Locate every blood parasite and identify its species.
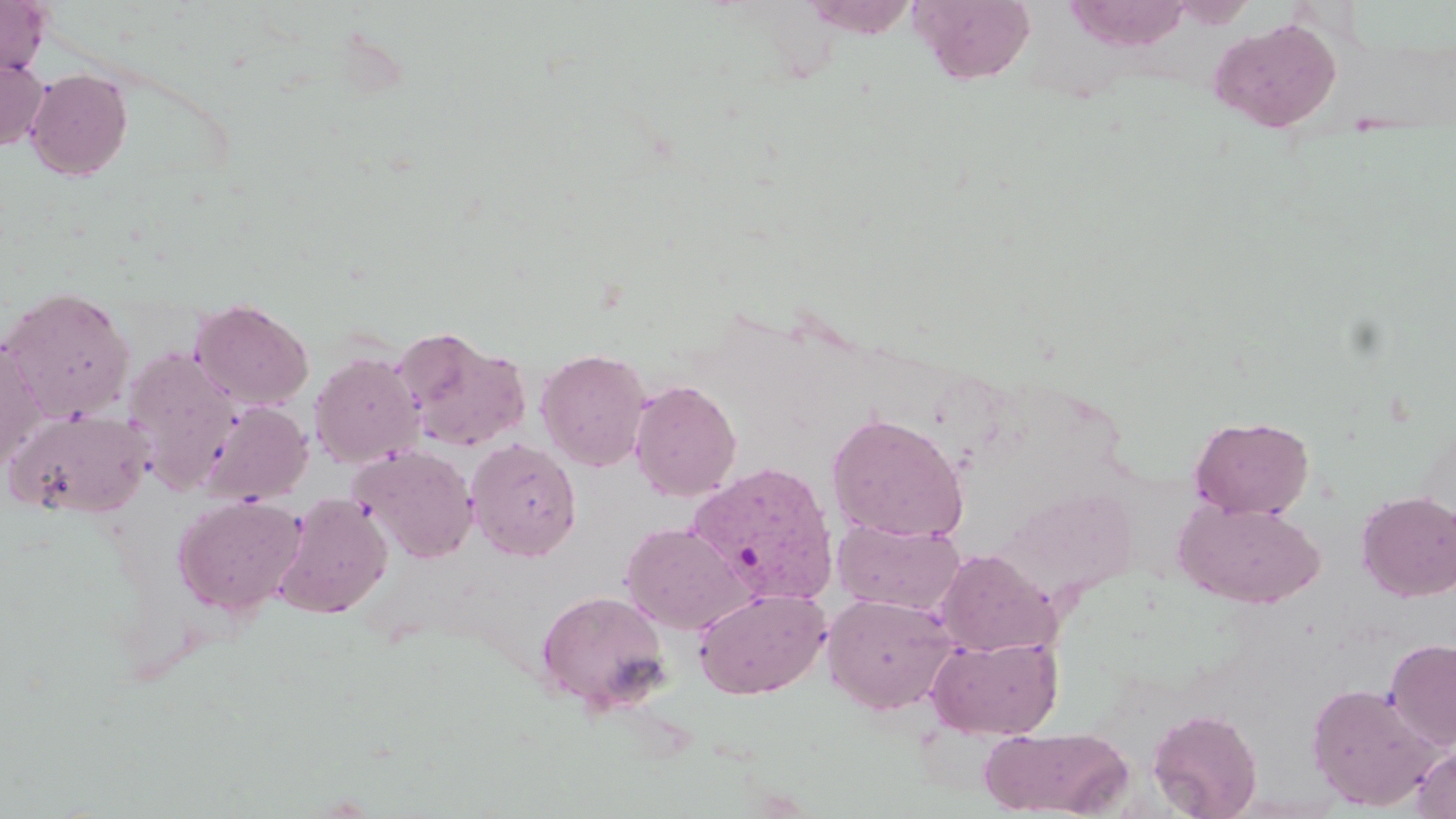

Approximate bounding boxes as [x1, y1, x2, y2] in pixels.
Plasmodium vivax-infected red blood cells: [687, 461, 839, 606].
No Plasmodium falciparum, Plasmodium ovale, Plasmodium malariae, Babesia divergens, or Trypanosoma brucei observed.

slide_level_diagnosis: Plasmodium vivax
modality: optical microscopy
stain: May-Grünwald-Giemsa
preparation: thin blood smear
magnification: 1000x
uninfected_red_blood_cell_locations: 'approximate bounding boxes as [x1, y1, x2, y2] in pixels: [800, 0, 920, 39], [911, 0, 1037, 84], [0, 1, 51, 77], [1207, 17, 1344, 133], [0, 58, 49, 150], [24, 68, 132, 180], [0, 287, 136, 423], [191, 299, 314, 410], [395, 328, 532, 452], [0, 337, 47, 473], [122, 346, 241, 491], [535, 348, 651, 471], [309, 351, 424, 468], [629, 379, 742, 501], [199, 400, 313, 505], [5, 407, 153, 519], [827, 412, 969, 543], [1189, 415, 1314, 520], [466, 438, 582, 561], [350, 444, 480, 563], [999, 487, 1137, 600], [1357, 491, 1456, 601], [275, 493, 393, 618], [173, 494, 305, 617], [1175, 499, 1325, 608], [833, 517, 965, 616], [620, 522, 751, 634], [935, 548, 1061, 656], [693, 587, 830, 699], [536, 589, 671, 715], [822, 592, 962, 716], [927, 634, 1063, 739], [1385, 637, 1456, 750], [1307, 682, 1443, 810], [1148, 708, 1263, 819], [979, 726, 1131, 817], [1412, 740, 1456, 818]'
image_size: 1456×819 pixels
field_of_view: one of a larger specimen